Name the parasite shown.
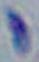
This is Toxoplasma gondii.

1000x magnification. Micrograph.